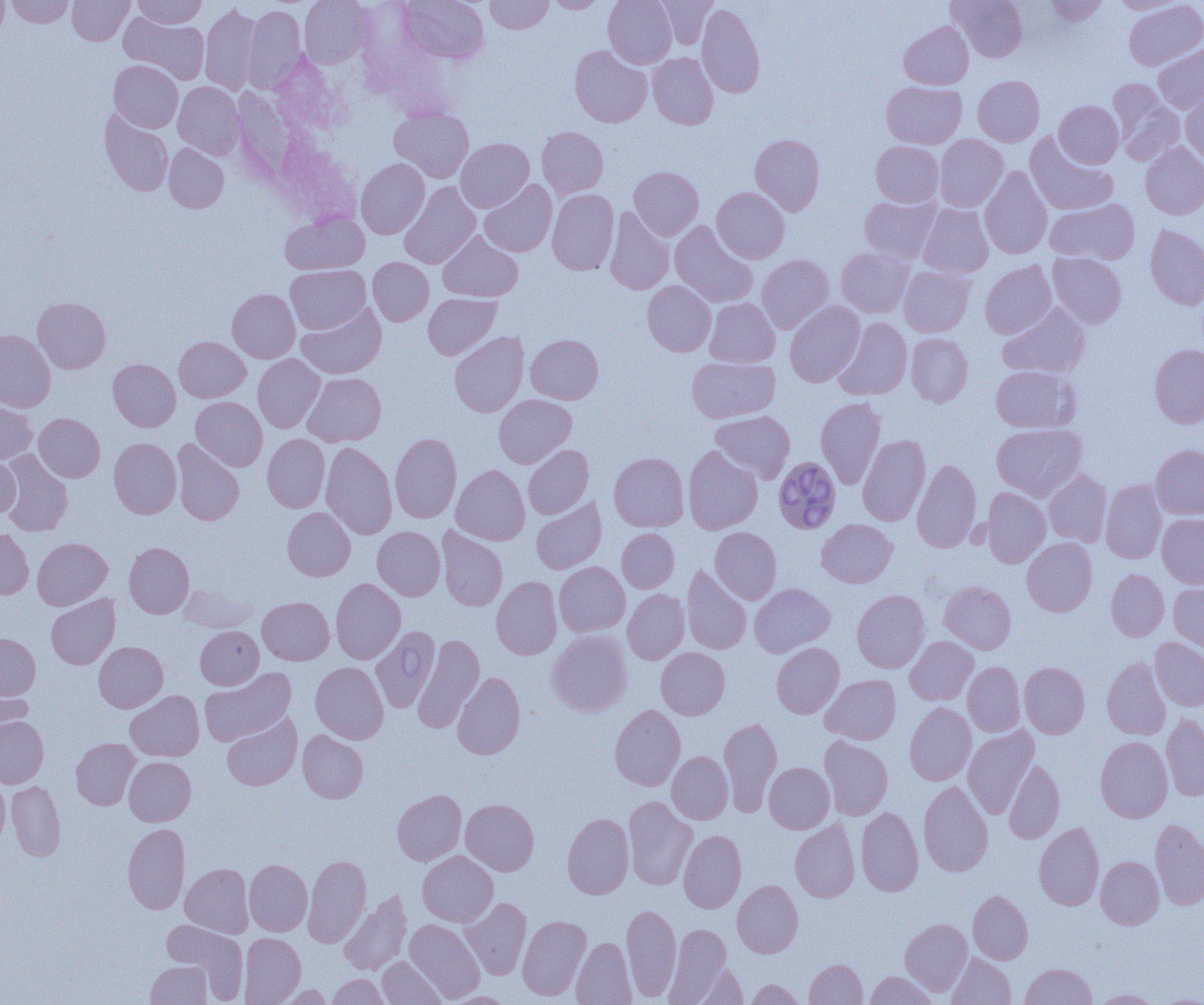

slide_level_diagnosis: Babesia divergens
field_of_view: single
preparation: thin blood smear
uninfected_red_blood_cell_locations: 'approximate bounding boxes as [x1, y1, x2, y2] in pixels: [0, 0, 8, 39], [6, 0, 75, 28], [68, 0, 133, 45], [134, 0, 206, 29], [299, 0, 373, 68], [400, 0, 488, 64], [485, 0, 553, 33], [544, 0, 608, 13], [603, 0, 677, 68], [653, 0, 718, 48], [948, 0, 1027, 62], [1044, 0, 1108, 26], [1109, 1, 1187, 14], [1124, 1, 1204, 70], [697, 3, 765, 99], [200, 5, 262, 94], [243, 5, 306, 92], [119, 13, 210, 84], [899, 21, 973, 89], [1153, 44, 1204, 113], [570, 45, 652, 127], [648, 53, 718, 129], [109, 60, 183, 132], [973, 75, 1044, 146], [1107, 80, 1184, 165], [173, 81, 244, 159], [882, 81, 966, 148], [1181, 87, 1204, 166], [1054, 100, 1123, 168], [389, 107, 473, 182], [100, 109, 174, 196], [537, 127, 608, 200], [1025, 133, 1117, 215], [750, 134, 825, 216], [934, 134, 1008, 211], [456, 138, 534, 212], [871, 140, 943, 207], [1140, 142, 1204, 219], [164, 144, 229, 212], [356, 158, 430, 239], [629, 166, 703, 240], [980, 166, 1052, 259], [480, 179, 557, 256], [399, 182, 481, 269], [712, 187, 790, 263], [547, 189, 619, 275], [859, 194, 941, 264], [1045, 199, 1139, 265], [917, 203, 993, 278], [604, 208, 674, 294], [281, 212, 369, 274], [670, 221, 758, 307], [1145, 225, 1204, 310], [438, 231, 523, 301], [836, 247, 914, 317], [1047, 253, 1126, 328], [756, 254, 834, 334], [368, 257, 433, 326], [980, 261, 1056, 338], [286, 265, 370, 333], [899, 266, 975, 337], [642, 281, 716, 356], [227, 289, 300, 362], [423, 293, 501, 360], [32, 297, 111, 373], [704, 297, 780, 367], [784, 301, 865, 387], [297, 302, 386, 378], [998, 303, 1090, 379], [833, 318, 912, 400], [0, 329, 55, 412], [449, 331, 528, 417], [906, 333, 973, 406], [526, 334, 603, 404], [174, 336, 250, 402], [1149, 344, 1204, 428], [253, 354, 324, 433], [686, 356, 780, 422], [108, 359, 180, 431], [990, 365, 1079, 433], [303, 372, 386, 447], [494, 394, 576, 467], [191, 397, 267, 471], [815, 397, 886, 489], [0, 400, 37, 464], [710, 410, 795, 483], [34, 413, 104, 482], [992, 423, 1087, 501], [390, 433, 461, 523], [262, 434, 329, 512], [858, 435, 930, 526], [109, 438, 182, 519], [172, 439, 244, 526], [321, 442, 397, 540], [1150, 444, 1204, 519], [523, 445, 593, 519], [683, 445, 763, 534], [1, 451, 73, 536], [609, 452, 689, 532], [0, 456, 20, 518], [912, 459, 981, 553], [451, 465, 530, 545], [1043, 469, 1112, 547], [1100, 480, 1167, 563], [981, 487, 1051, 568], [531, 497, 607, 574], [282, 507, 355, 581], [1157, 513, 1204, 588], [816, 519, 897, 588], [373, 526, 445, 600], [436, 526, 508, 611], [710, 527, 781, 603], [0, 528, 33, 599], [617, 528, 679, 593], [33, 538, 112, 610], [1022, 538, 1098, 616], [124, 542, 194, 618], [554, 562, 630, 636], [682, 566, 751, 654], [1106, 569, 1169, 641], [491, 576, 562, 659], [331, 578, 405, 664], [938, 580, 1016, 654], [1168, 582, 1204, 655], [180, 583, 257, 632], [750, 583, 836, 657], [623, 589, 689, 664], [852, 590, 930, 673], [46, 595, 120, 669], [258, 597, 334, 665], [195, 626, 263, 689], [371, 626, 440, 712], [547, 630, 632, 717], [0, 633, 41, 701], [413, 633, 485, 732], [905, 636, 978, 705], [1150, 638, 1204, 711], [94, 641, 168, 712], [771, 642, 844, 718], [656, 647, 730, 719], [1102, 656, 1171, 740], [963, 661, 1025, 737], [311, 662, 389, 744], [1019, 662, 1090, 738], [200, 667, 295, 746], [453, 672, 525, 759], [820, 674, 901, 744], [0, 686, 34, 745], [126, 690, 204, 761], [905, 703, 976, 785], [609, 705, 685, 791], [222, 713, 302, 790], [1161, 713, 1204, 801], [0, 716, 48, 787], [719, 717, 782, 816], [963, 726, 1038, 818], [298, 730, 368, 803], [819, 736, 893, 820], [1095, 736, 1172, 822], [71, 738, 140, 809], [667, 751, 733, 824], [124, 756, 195, 825], [1004, 760, 1064, 843], [764, 762, 834, 833], [0, 775, 9, 849], [7, 780, 66, 861], [918, 781, 993, 877], [392, 789, 466, 865], [623, 797, 697, 890], [461, 799, 539, 875], [856, 807, 923, 896], [562, 813, 634, 899], [1150, 818, 1204, 910], [790, 819, 859, 902], [1034, 822, 1104, 910], [123, 823, 189, 914], [679, 831, 746, 912], [418, 850, 498, 926], [303, 855, 371, 947], [1096, 856, 1164, 929], [244, 859, 312, 936], [180, 863, 253, 938], [732, 880, 803, 957], [968, 890, 1033, 964], [339, 892, 412, 975], [461, 898, 532, 979], [622, 903, 681, 1001], [517, 914, 591, 1001], [900, 918, 972, 995], [405, 919, 485, 1002], [161, 920, 247, 999], [664, 922, 732, 1004], [239, 932, 306, 1004], [571, 937, 636, 1004], [947, 953, 1016, 1004], [378, 957, 446, 1005], [804, 959, 867, 1005], [145, 960, 212, 1004], [685, 963, 748, 1004], [1020, 963, 1096, 1005], [865, 972, 938, 1004], [327, 973, 388, 1005], [746, 979, 805, 1004], [272, 984, 334, 1004], [1090, 989, 1162, 1004], [443, 992, 515, 1005]'
modality: light microscopy
image_size: 1204×1005 pixels
babesia_divergens_infected_red_blood_cell_locations: 'approximate bounding boxes as [x1, y1, x2, y2] in pixels: [776, 458, 844, 536]'
magnification: 1000x